Identify the parasite.
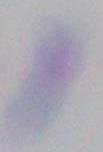

This is Toxoplasma gondii.

Summary:
  - Modality: micrograph
  - Magnification: 1000x